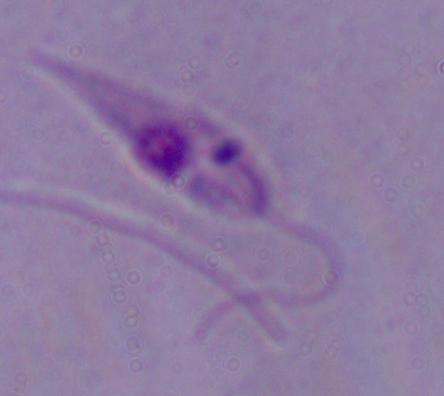
Summary:
  - Identification: Leishmania
  - Magnification: 1000x
  - Modality: micrograph